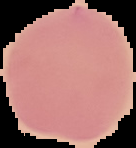 Image is 136×148 pixels. Malaria status: uninfected. From a thin blood smear. Segmented cell region on a black background.